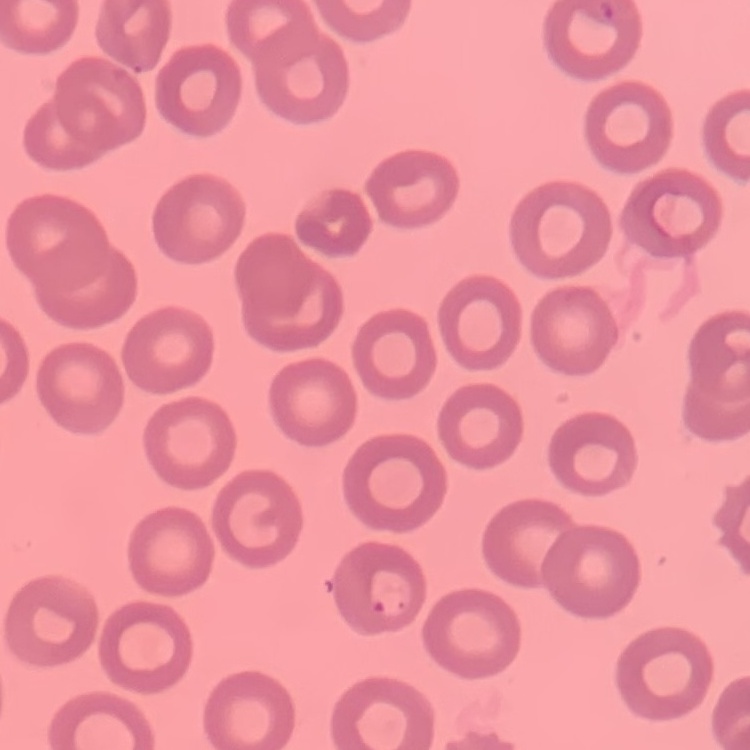

{
  "red_blood_cell_morphology": "no rouleaux formation",
  "image_type": "square crop of a larger photomicrograph",
  "preparation": "thin blood film",
  "stain": "Field's or Giemsa"
}